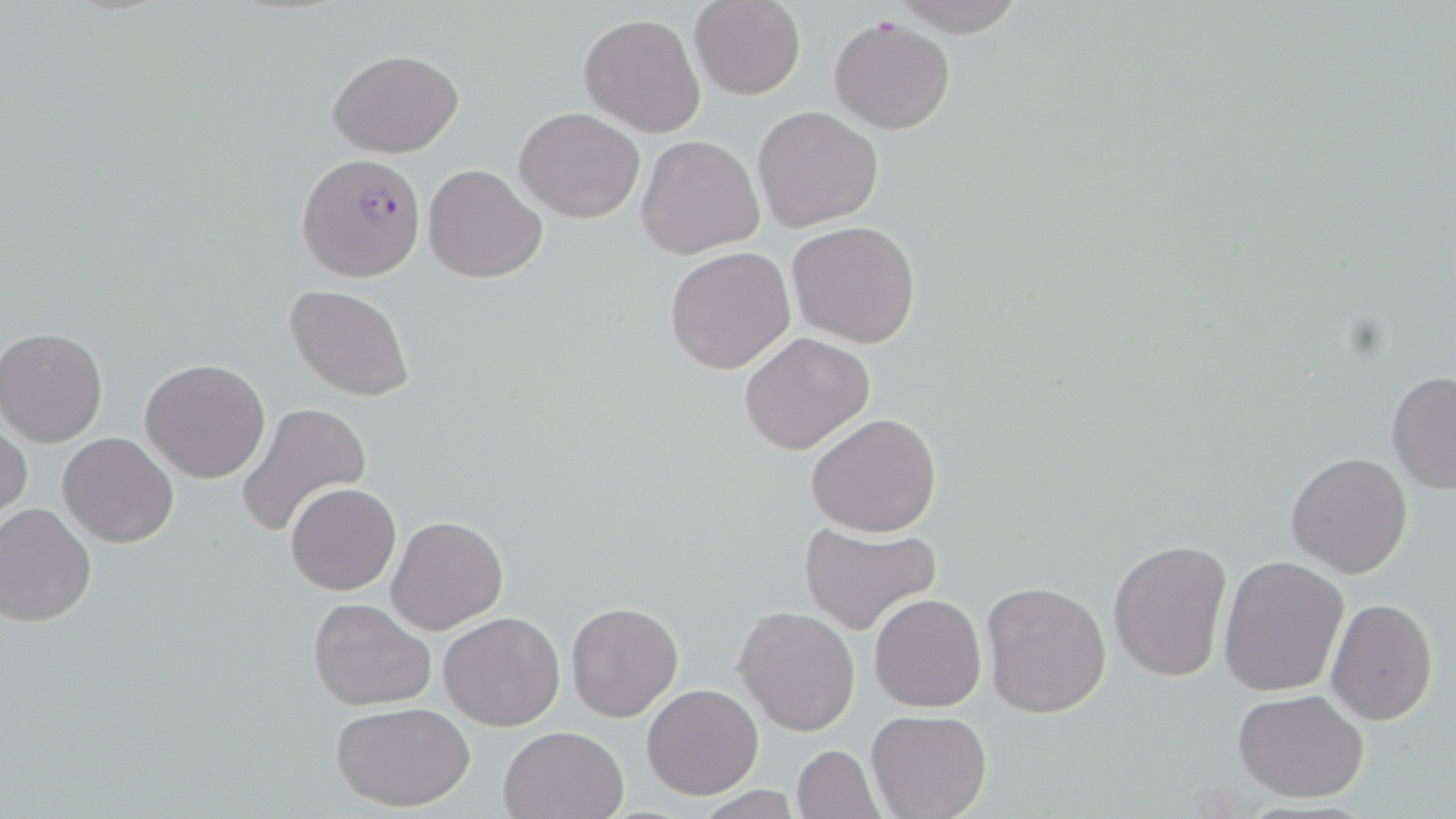 Approximate bounding boxes as (x1, y1, x2, y2) in pixels. Uninfected red blood cell locations: (688, 1, 805, 99), (885, 1, 1031, 35), (578, 13, 706, 138), (829, 16, 957, 133), (328, 48, 464, 158), (754, 106, 882, 232), (515, 107, 644, 223), (635, 135, 764, 259), (422, 164, 546, 282), (788, 221, 921, 348), (665, 246, 796, 375), (285, 283, 416, 402), (0, 326, 109, 447), (738, 332, 876, 457), (140, 358, 271, 483), (1386, 370, 1455, 493), (235, 402, 371, 540), (1, 412, 31, 525), (805, 412, 944, 537), (57, 432, 180, 548), (1286, 452, 1413, 578), (286, 482, 401, 596), (0, 503, 97, 627), (386, 515, 509, 635), (797, 519, 943, 638), (1108, 538, 1231, 684), (1218, 554, 1350, 696), (981, 581, 1112, 718), (869, 593, 987, 713), (308, 597, 436, 711), (1326, 598, 1438, 725), (566, 600, 684, 721), (733, 605, 860, 737), (439, 611, 567, 731), (641, 682, 765, 800), (1233, 688, 1370, 802), (331, 701, 475, 812), (867, 710, 992, 819), (498, 726, 628, 819), (791, 745, 883, 819). Plasmodium falciparum-infected red blood cell locations: (296, 152, 425, 282). Slide-level diagnosis: Plasmodium falciparum. One field of a larger specimen. Thin blood smear. Captured at 1000x magnification. Image is 1456×819 pixels. May-Grünwald-Giemsa-stained preparation. Optical microscopy.